Classify this cell by malaria status.
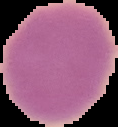

Uninfected.

Summary:
  - Preparation: thin blood film
  - Image type: segmented cell region on a black background
  - Image size: 118×127 pixels